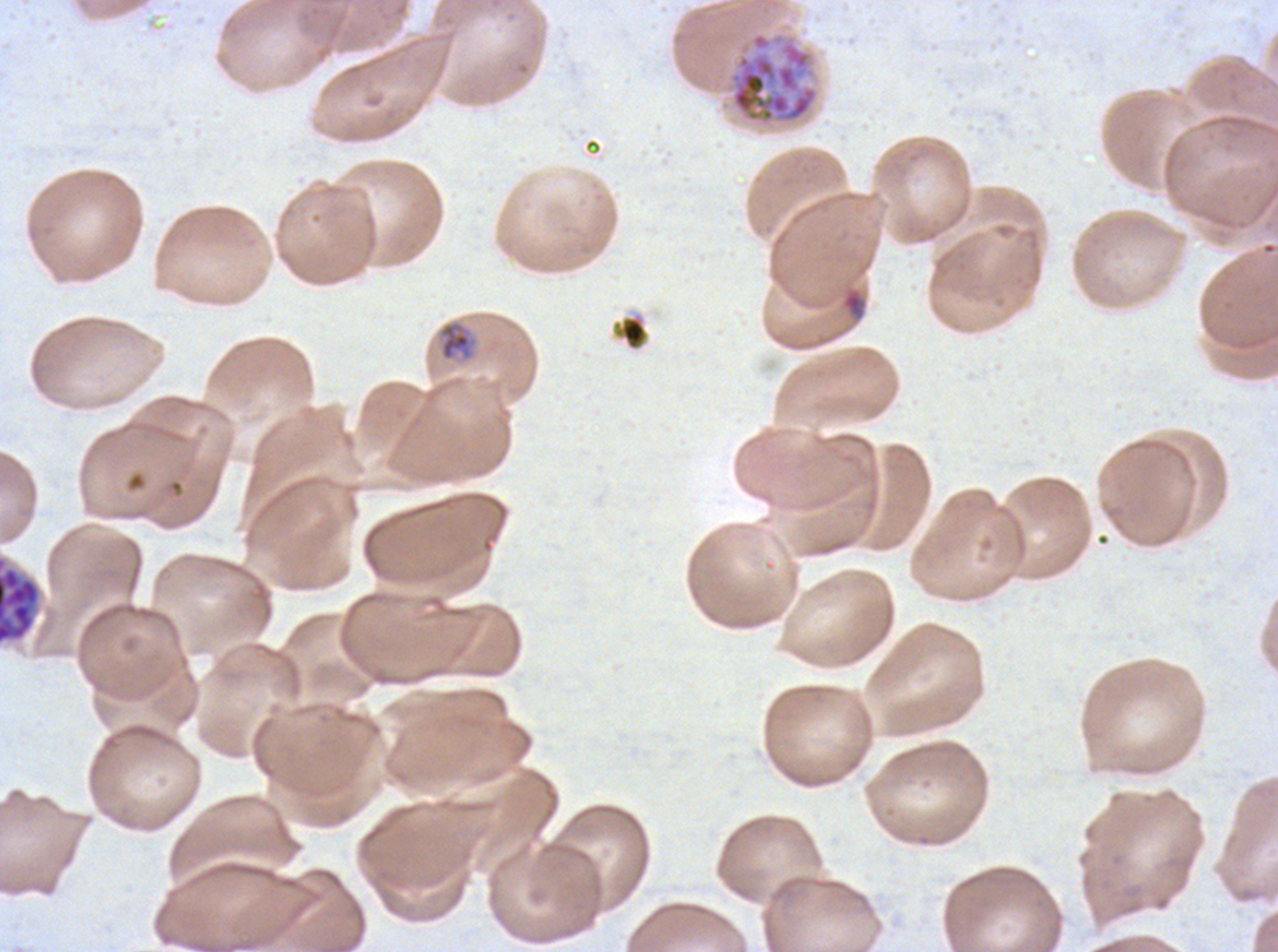 Approximate bounding rectangles given as corner coordinates in pixels from the top-left. Late schizont locations: (x1=728, y1=31, x2=820, y2=128), (x1=0, y1=555, x2=42, y2=645). Late-ring/early-trophozoite locations: (x1=437, y1=320, x2=475, y2=362). Debris locations: (x1=612, y1=314, x2=649, y2=351). Ring locations: (x1=841, y1=287, x2=866, y2=320). Giemsa stain. Thin blood smear. Life-cycle stages observed: ring, late-ring/early-trophozoite, late schizont. Image is 1278×952 pixels. P. falciparum from a patient in The Gambia, cultured ex vivo for 24 to 48 hours. One sub-image of a larger composite.